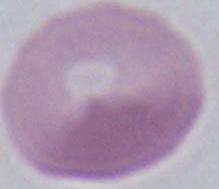
Summary:
  - Magnification: 1000x
  - Identification: erythrocyte
  - Modality: micrograph